Outline each blood parasite and name the species.
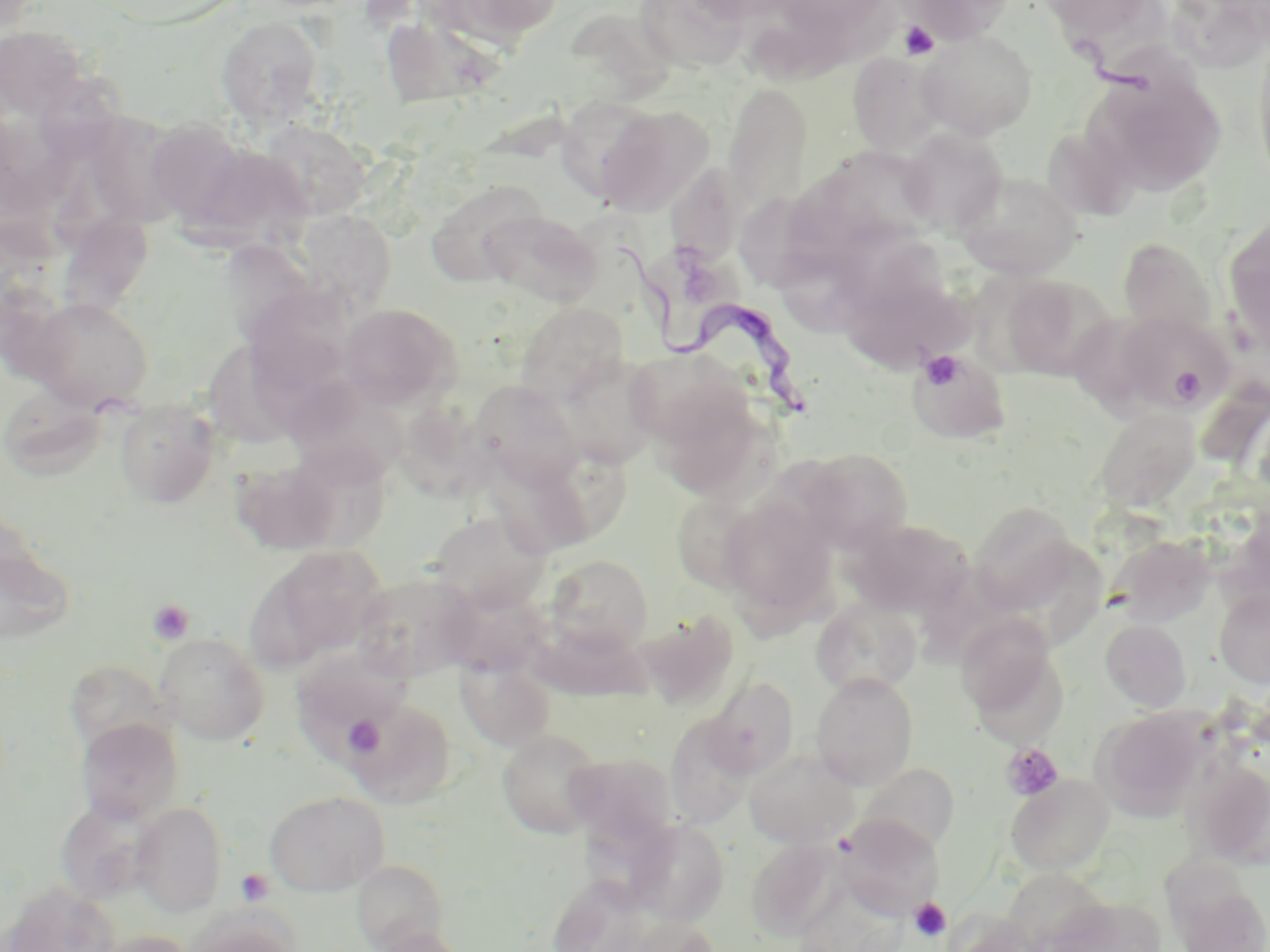

Approximate bounding boxes as (x1, y1, x2, y2) in pixels.
Trypanosoma brucei: (618, 244, 824, 427).
No Plasmodium falciparum, Plasmodium ovale, Plasmodium malariae, Plasmodium vivax, or Babesia divergens observed.

Platelet locations: (898, 20, 941, 60), (920, 351, 965, 389), (1170, 365, 1207, 404), (147, 599, 194, 646), (344, 714, 383, 756), (1001, 743, 1064, 802), (235, 868, 274, 906), (909, 898, 951, 942). Uninfected red blood cell locations: (427, 0, 565, 49), (634, 0, 755, 73), (772, 0, 891, 41), (900, 0, 1017, 42), (1035, 0, 1158, 40), (215, 16, 327, 128), (0, 28, 98, 117), (384, 30, 516, 114), (917, 31, 1038, 139), (1252, 40, 1270, 194), (848, 51, 947, 156), (1089, 69, 1227, 196), (724, 84, 813, 216), (562, 96, 657, 191), (595, 103, 713, 215), (78, 110, 173, 213), (0, 113, 81, 216), (144, 118, 247, 223), (256, 119, 371, 219), (1041, 122, 1140, 221), (898, 128, 1007, 234), (186, 142, 315, 253), (676, 154, 746, 266), (954, 169, 1083, 278), (796, 170, 892, 280), (424, 180, 545, 286), (739, 190, 823, 293), (55, 203, 155, 317), (481, 209, 601, 307), (292, 210, 398, 316), (1224, 218, 1270, 353), (842, 220, 951, 323), (1117, 237, 1217, 333), (225, 243, 332, 361), (646, 249, 741, 338), (1001, 275, 1114, 381), (846, 289, 986, 366), (25, 296, 154, 411), (251, 298, 369, 395), (514, 301, 629, 404), (339, 303, 462, 409), (1115, 312, 1236, 411), (209, 345, 300, 447), (624, 347, 756, 457), (910, 349, 1010, 444), (557, 354, 664, 470), (286, 380, 408, 487), (470, 381, 585, 490), (2, 387, 112, 481), (114, 399, 220, 508), (401, 404, 506, 511), (1093, 407, 1200, 513), (277, 445, 395, 554), (488, 445, 634, 560), (795, 448, 913, 554), (231, 457, 344, 556), (671, 489, 765, 594), (720, 497, 837, 628), (969, 502, 1079, 609), (428, 510, 552, 611), (846, 518, 973, 617), (1110, 534, 1215, 629), (0, 539, 76, 645), (252, 544, 389, 666), (544, 554, 654, 657), (351, 570, 478, 682), (439, 582, 549, 677), (1214, 589, 1270, 688), (811, 597, 923, 697), (633, 610, 739, 711), (957, 612, 1064, 730), (1100, 618, 1191, 711), (531, 623, 652, 702), (154, 632, 270, 745), (292, 649, 413, 751), (456, 657, 555, 752), (61, 669, 172, 749), (811, 672, 918, 790), (703, 676, 800, 780), (345, 698, 457, 808), (1093, 707, 1210, 821), (665, 713, 755, 828), (75, 718, 184, 824), (496, 728, 607, 839), (745, 747, 859, 849), (564, 752, 679, 850), (1183, 755, 1270, 869), (858, 763, 961, 857), (1005, 774, 1114, 875), (264, 790, 389, 897), (54, 798, 156, 905), (130, 802, 228, 916), (835, 815, 944, 919), (627, 819, 730, 924), (747, 838, 844, 941), (351, 861, 450, 949), (1164, 864, 1270, 951), (2, 882, 122, 952), (1048, 895, 1165, 952), (182, 912, 301, 952), (621, 917, 721, 952), (368, 926, 472, 952), (91, 929, 196, 952). Slide-level diagnosis: Trypanosoma brucei. Thin blood film. Light microscopy. 1000x magnification. Image is 1270×952 pixels. Single field of view. May-Grünwald-Giemsa stain.